State which cell type is depicted.
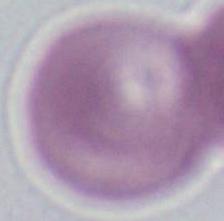

This is an erythrocyte.

{
  "modality": "micrograph",
  "magnification": "1000x"
}